Locate and identify every blood parasite.
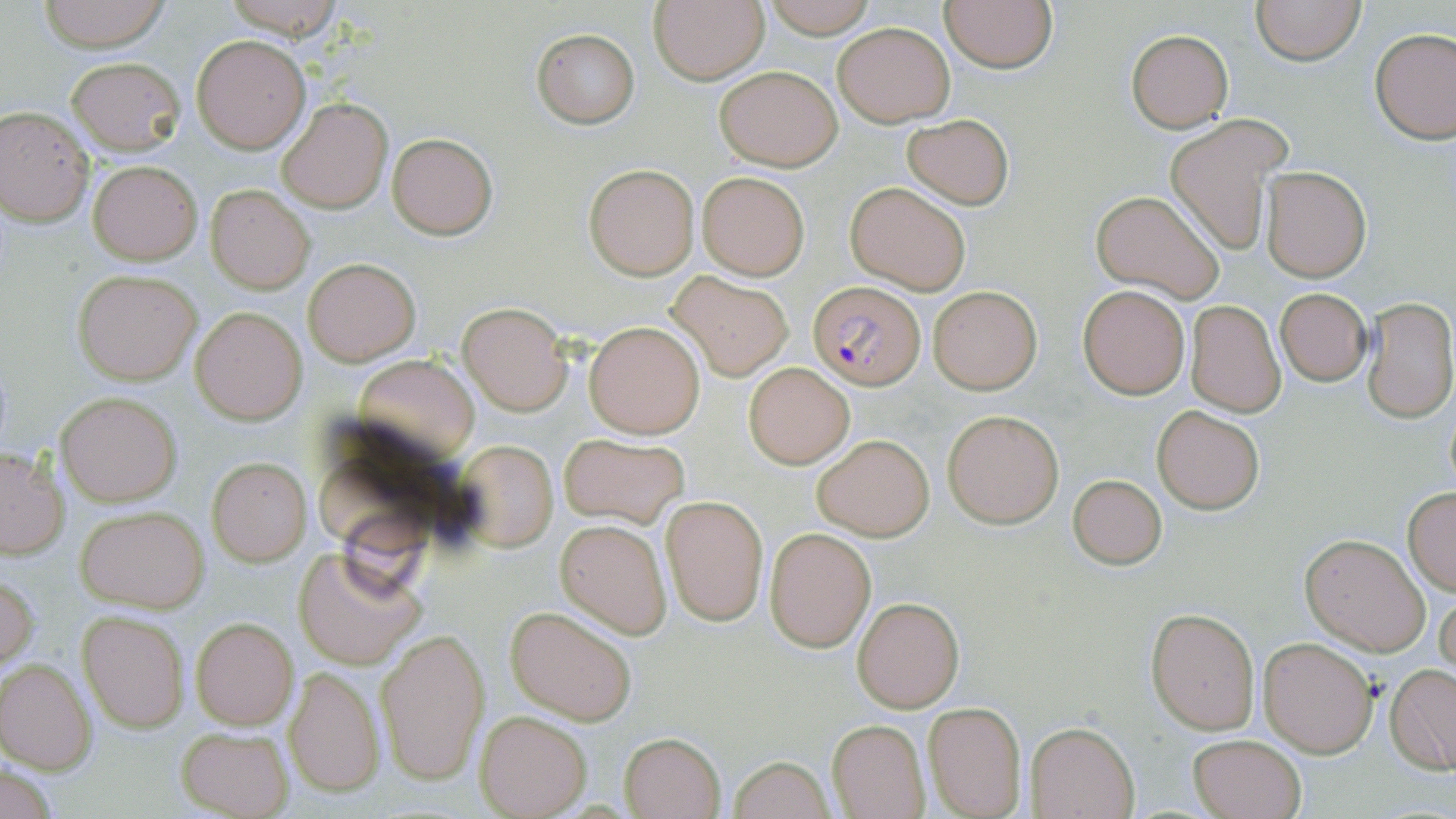

Approximate bounding boxes as (x1, y1, x2, y2) in pixels.
Plasmodium falciparum-infected red blood cells: (809, 281, 926, 388).
No Plasmodium ovale, Plasmodium malariae, Plasmodium vivax, Babesia divergens, or Trypanosoma brucei observed.

Summary:
  - Uninfected red blood cell locations: (38, 0, 171, 51), (219, 0, 347, 37), (763, 0, 877, 39), (939, 0, 1057, 72), (1251, 0, 1365, 65), (650, 2, 769, 84), (833, 21, 955, 127), (532, 29, 639, 128), (1370, 29, 1456, 144), (1126, 31, 1233, 131), (191, 34, 311, 153), (66, 56, 184, 156), (714, 65, 842, 170), (277, 98, 393, 215), (0, 106, 95, 226), (901, 113, 1014, 208), (1166, 114, 1285, 255), (388, 133, 497, 239), (89, 161, 201, 265), (584, 164, 700, 280), (1261, 166, 1371, 281), (697, 172, 809, 280), (845, 181, 972, 294), (205, 184, 315, 294), (1089, 190, 1227, 305), (303, 258, 420, 366), (73, 269, 202, 384), (669, 272, 793, 380), (1078, 284, 1190, 399), (928, 285, 1043, 395), (1274, 288, 1373, 385), (1361, 296, 1455, 423), (1186, 300, 1286, 417), (459, 303, 573, 416), (191, 308, 307, 424), (584, 320, 706, 438), (353, 355, 479, 464), (743, 360, 856, 469), (56, 391, 181, 507), (1442, 393, 1456, 499), (1152, 405, 1264, 514), (944, 409, 1061, 527), (813, 432, 933, 541), (559, 433, 690, 527), (453, 440, 559, 550), (0, 447, 69, 560), (206, 458, 312, 566), (1067, 472, 1168, 570), (1402, 487, 1456, 596), (661, 495, 768, 624), (75, 506, 208, 612), (556, 519, 672, 638), (765, 528, 876, 651), (1300, 533, 1430, 656), (293, 545, 428, 671), (0, 573, 39, 673), (1435, 587, 1456, 686), (853, 597, 964, 712), (505, 606, 639, 726), (1146, 607, 1260, 734), (79, 611, 189, 732), (191, 618, 297, 729), (376, 630, 486, 786), (1259, 637, 1378, 756), (0, 658, 96, 774), (1386, 664, 1456, 774), (284, 665, 385, 800), (922, 701, 1027, 818), (476, 711, 592, 817), (827, 719, 931, 819), (1027, 721, 1139, 818), (176, 725, 292, 818), (620, 731, 725, 818), (1187, 732, 1307, 819), (728, 754, 836, 819)
  - Slide-level diagnosis: Plasmodium falciparum
  - Preparation: thin blood film
  - Image size: 1456×819 pixels
  - Stain: May-Grünwald-Giemsa
  - Modality: optical microscopy
  - Field of view: one of a larger specimen
  - Magnification: 1000x